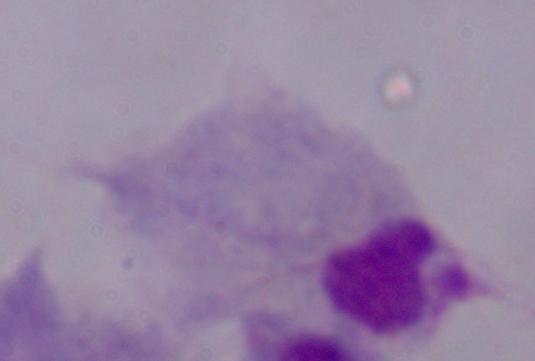

magnification = 1000x
modality = photomicrograph
identification = trichomonad